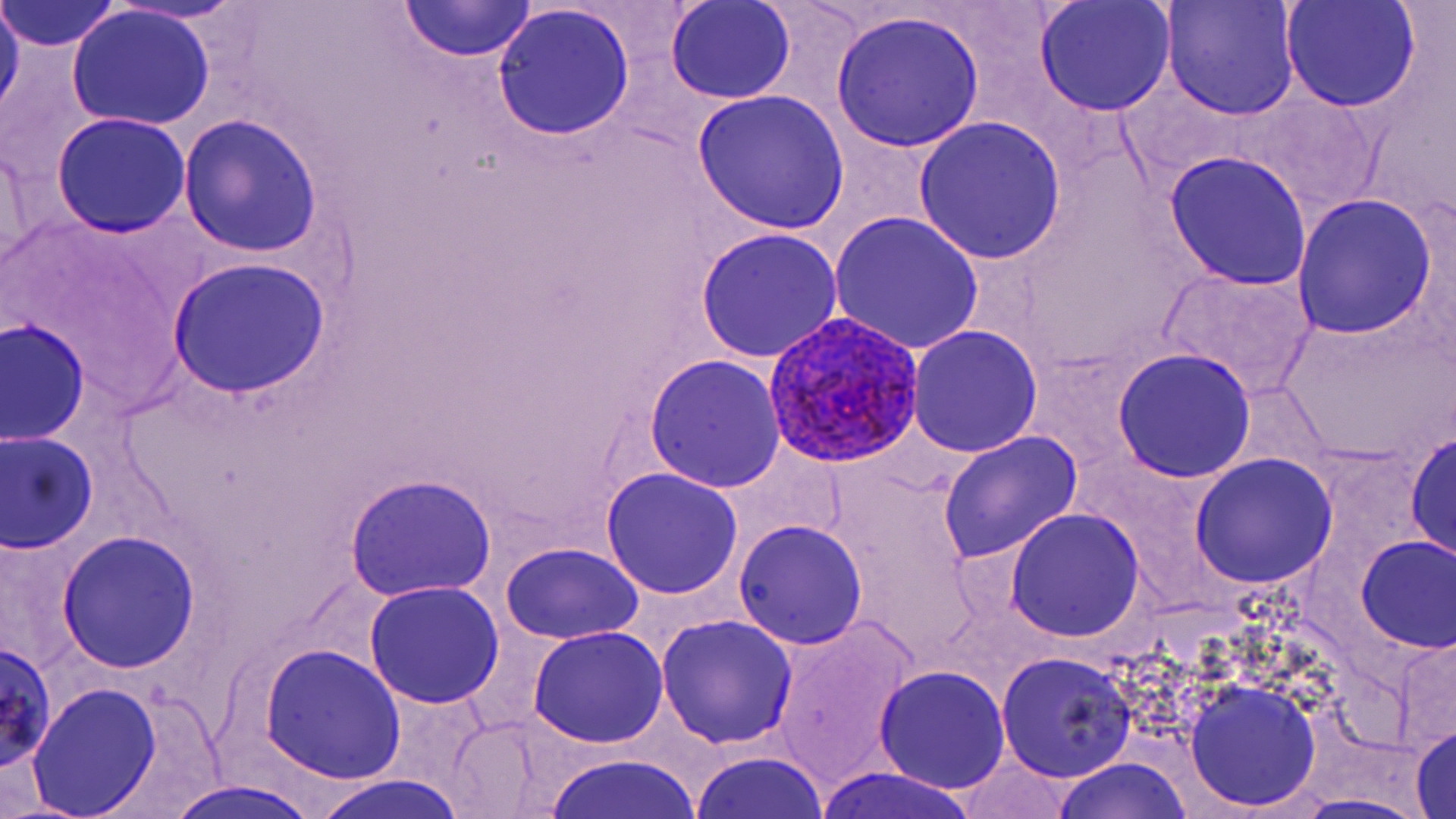
Approximate bounding boxes as [x1, y1, x2, y2] in pixels. Plasmodium ovale-infected red blood cell locations: [764, 314, 924, 467]. Uninfected red blood cell locations: [0, 0, 23, 126], [394, 0, 539, 65], [1161, 0, 1300, 121], [1279, 0, 1422, 113], [109, 1, 251, 26], [664, 1, 797, 105], [1032, 1, 1177, 117], [2, 2, 123, 54], [492, 5, 633, 142], [66, 8, 217, 131], [831, 13, 986, 151], [690, 88, 853, 234], [50, 113, 191, 237], [178, 116, 321, 259], [913, 116, 1067, 264], [0, 137, 38, 277], [1164, 152, 1312, 290], [1292, 193, 1438, 342], [826, 211, 986, 356], [694, 227, 845, 363], [169, 256, 330, 400], [1157, 268, 1317, 397], [1271, 307, 1452, 469], [2, 319, 91, 444], [906, 325, 1043, 458], [1112, 347, 1256, 483], [643, 355, 786, 492], [1406, 429, 1455, 561], [1, 431, 98, 553], [936, 431, 1084, 566], [1189, 453, 1338, 591], [600, 468, 743, 598], [343, 475, 498, 602], [1004, 509, 1146, 642], [734, 520, 867, 649], [58, 530, 200, 672], [1353, 535, 1456, 654], [499, 544, 642, 645], [363, 581, 504, 709], [656, 614, 798, 749], [771, 618, 922, 792], [527, 627, 669, 749], [1393, 636, 1456, 756], [0, 641, 57, 770], [256, 642, 409, 784], [998, 652, 1137, 782], [873, 665, 1010, 794], [1183, 680, 1322, 813], [27, 683, 163, 818], [446, 718, 561, 816], [1411, 724, 1455, 819], [690, 749, 834, 819], [542, 751, 708, 819], [952, 754, 1080, 818], [1045, 757, 1198, 819], [815, 766, 983, 819], [310, 774, 468, 819], [163, 779, 321, 819], [1283, 792, 1437, 819]. Slide-level diagnosis: Plasmodium ovale. 1000x magnification. Image is 1456×819 pixels. Thin blood smear. May-Grünwald-Giemsa-stained preparation. Optical microscopy. One field of a larger specimen.